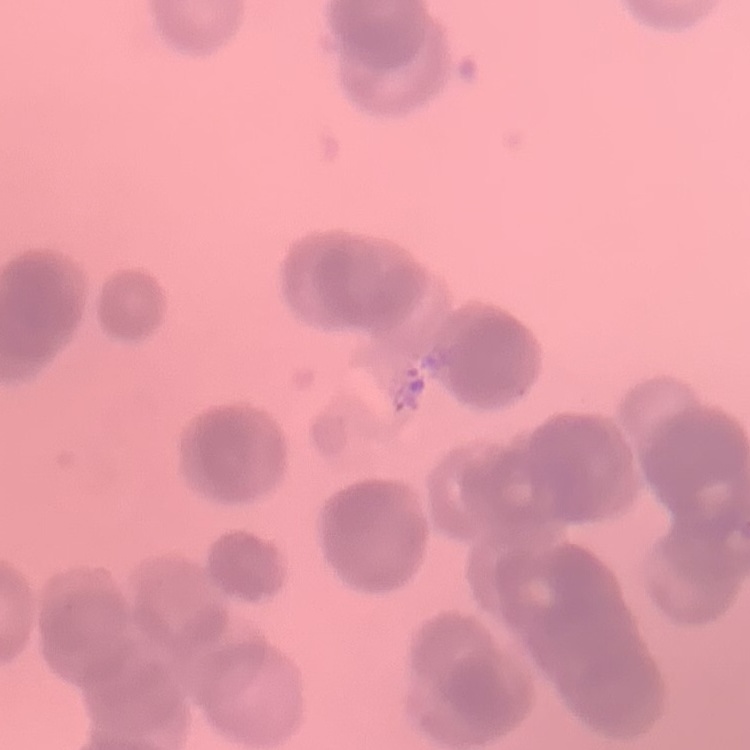

The erythrocytes show rouleaux formation. Thin blood smear. Square crop of a larger photomicrograph. Field's or Giemsa stain.